Name the parasite shown.
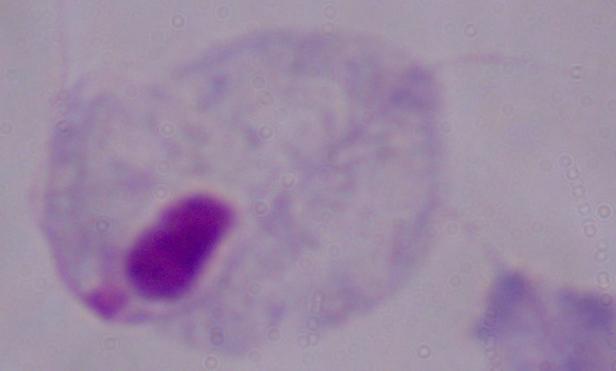
A trichomonad.

1000x magnification. Micrograph.